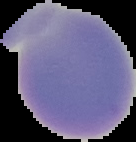 Segmented cell region on a black background. Result: negative for Plasmodium parasites. Image is 136×142 pixels. From a thin blood film.